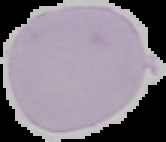
image_size: 166×142 pixels
preparation: thin blood smear
image_type: segmented cell region on a black background
malaria_status: uninfected